Locate every blood parasite and identify its species.
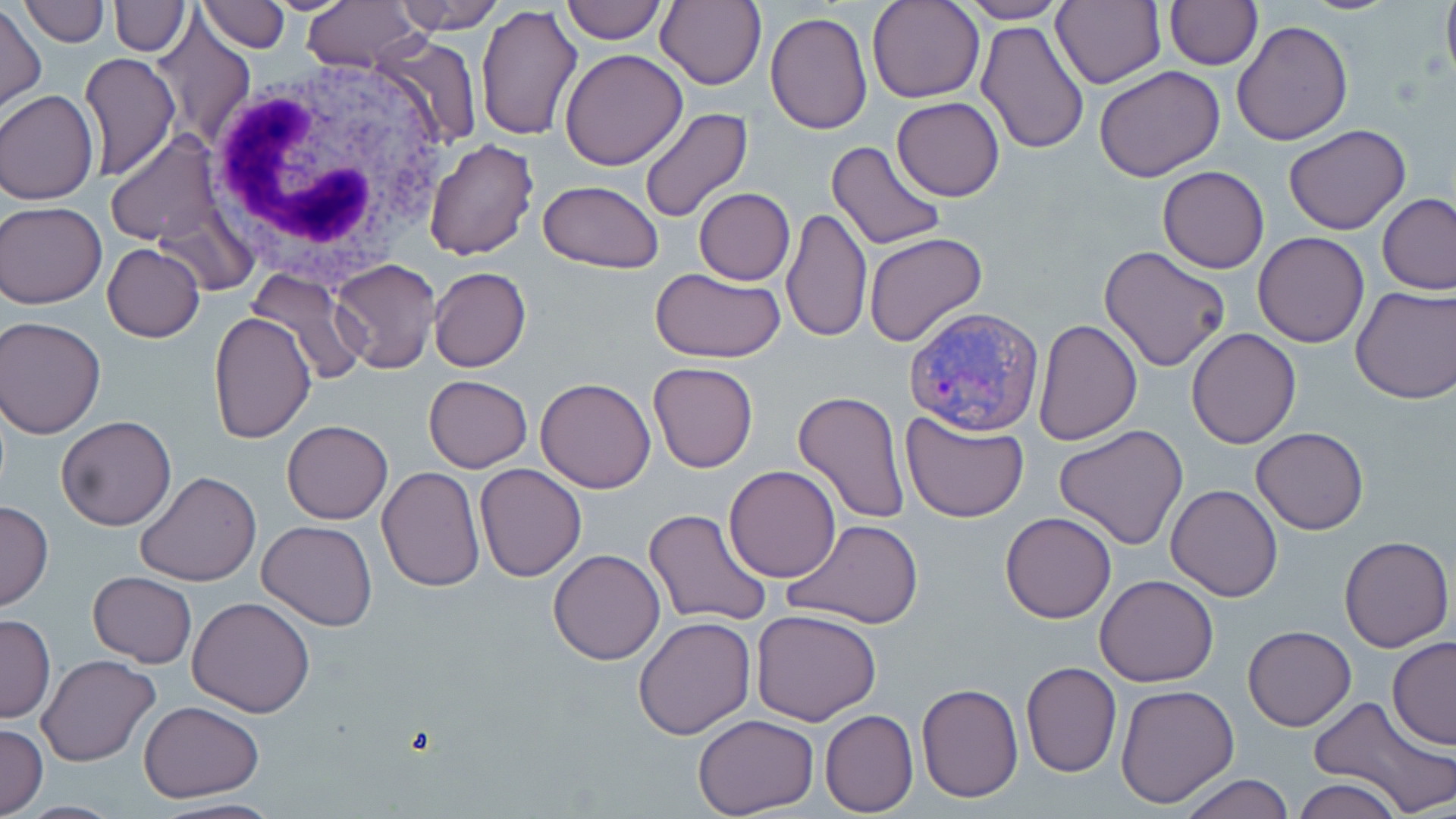

Approximate bounding boxes as named x1/y1/x2/y2 corners in pixels.
Plasmodium vivax-infected red blood cells: (x1=904, y1=307, x2=1043, y2=437).
No Plasmodium falciparum, Plasmodium ovale, Plasmodium malariae, Babesia divergens, or Trypanosoma brucei observed.

Summary:
  - White blood cell locations: (x1=201, y1=56, x2=460, y2=289)
  - Uninfected red blood cell locations: (x1=23, y1=0, x2=109, y2=46), (x1=112, y1=0, x2=188, y2=56), (x1=198, y1=0, x2=291, y2=52), (x1=254, y1=0, x2=360, y2=15), (x1=300, y1=0, x2=422, y2=72), (x1=394, y1=0, x2=502, y2=35), (x1=560, y1=0, x2=666, y2=44), (x1=866, y1=0, x2=985, y2=103), (x1=953, y1=0, x2=1071, y2=23), (x1=1440, y1=0, x2=1456, y2=85), (x1=654, y1=1, x2=766, y2=89), (x1=1051, y1=1, x2=1166, y2=88), (x1=1165, y1=2, x2=1262, y2=70), (x1=476, y1=3, x2=585, y2=142), (x1=0, y1=5, x2=45, y2=112), (x1=764, y1=11, x2=874, y2=135), (x1=153, y1=14, x2=255, y2=146), (x1=975, y1=20, x2=1089, y2=154), (x1=1233, y1=20, x2=1352, y2=145), (x1=374, y1=35, x2=480, y2=153), (x1=560, y1=48, x2=688, y2=170), (x1=79, y1=53, x2=180, y2=180), (x1=1094, y1=64, x2=1226, y2=182), (x1=1, y1=91, x2=99, y2=204), (x1=892, y1=98, x2=1004, y2=201), (x1=638, y1=108, x2=754, y2=225), (x1=1285, y1=124, x2=1411, y2=235), (x1=105, y1=132, x2=231, y2=252), (x1=423, y1=138, x2=539, y2=262), (x1=825, y1=140, x2=947, y2=252), (x1=1158, y1=166, x2=1269, y2=273), (x1=537, y1=179, x2=664, y2=273), (x1=693, y1=188, x2=795, y2=285), (x1=1379, y1=193, x2=1456, y2=294), (x1=2, y1=202, x2=106, y2=308), (x1=782, y1=208, x2=872, y2=342), (x1=1253, y1=232, x2=1369, y2=348), (x1=864, y1=233, x2=987, y2=349), (x1=102, y1=244, x2=205, y2=342), (x1=1099, y1=245, x2=1232, y2=372), (x1=330, y1=257, x2=440, y2=373), (x1=429, y1=267, x2=530, y2=372), (x1=651, y1=267, x2=786, y2=362), (x1=249, y1=271, x2=365, y2=386), (x1=1350, y1=284, x2=1456, y2=402), (x1=208, y1=313, x2=317, y2=444), (x1=1, y1=316, x2=106, y2=438), (x1=1033, y1=318, x2=1142, y2=445), (x1=1186, y1=328, x2=1300, y2=447), (x1=648, y1=361, x2=758, y2=473), (x1=423, y1=375, x2=532, y2=473), (x1=537, y1=378, x2=655, y2=493), (x1=791, y1=389, x2=909, y2=524), (x1=900, y1=410, x2=1030, y2=523), (x1=55, y1=415, x2=177, y2=531), (x1=282, y1=420, x2=392, y2=523), (x1=1053, y1=425, x2=1188, y2=550), (x1=1250, y1=426, x2=1370, y2=533), (x1=475, y1=464, x2=586, y2=581), (x1=723, y1=465, x2=843, y2=583), (x1=377, y1=467, x2=484, y2=591), (x1=134, y1=471, x2=260, y2=587), (x1=1166, y1=484, x2=1283, y2=601), (x1=0, y1=499, x2=54, y2=612), (x1=644, y1=508, x2=772, y2=629), (x1=1000, y1=512, x2=1117, y2=623), (x1=258, y1=520, x2=378, y2=631), (x1=783, y1=520, x2=924, y2=630), (x1=1338, y1=535, x2=1453, y2=653), (x1=548, y1=549, x2=665, y2=665), (x1=87, y1=572, x2=197, y2=667), (x1=1096, y1=575, x2=1219, y2=687), (x1=187, y1=597, x2=315, y2=718), (x1=751, y1=608, x2=882, y2=727), (x1=0, y1=615, x2=55, y2=723), (x1=633, y1=615, x2=756, y2=740), (x1=1241, y1=625, x2=1357, y2=731), (x1=1388, y1=638, x2=1456, y2=747), (x1=37, y1=654, x2=162, y2=767), (x1=1020, y1=661, x2=1122, y2=778), (x1=917, y1=684, x2=1022, y2=802), (x1=1115, y1=684, x2=1239, y2=809), (x1=1307, y1=694, x2=1455, y2=818), (x1=139, y1=701, x2=264, y2=801), (x1=820, y1=710, x2=918, y2=816), (x1=691, y1=714, x2=819, y2=818), (x1=0, y1=722, x2=47, y2=818), (x1=1175, y1=774, x2=1296, y2=819), (x1=1292, y1=777, x2=1402, y2=819), (x1=143, y1=798, x2=284, y2=819)
  - Slide-level diagnosis: Plasmodium vivax
  - Modality: light microscopy
  - Stain: May-Grünwald-Giemsa
  - Preparation: thin blood smear
  - Magnification: 1000x
  - Field of view: single
  - Image size: 1456×819 pixels